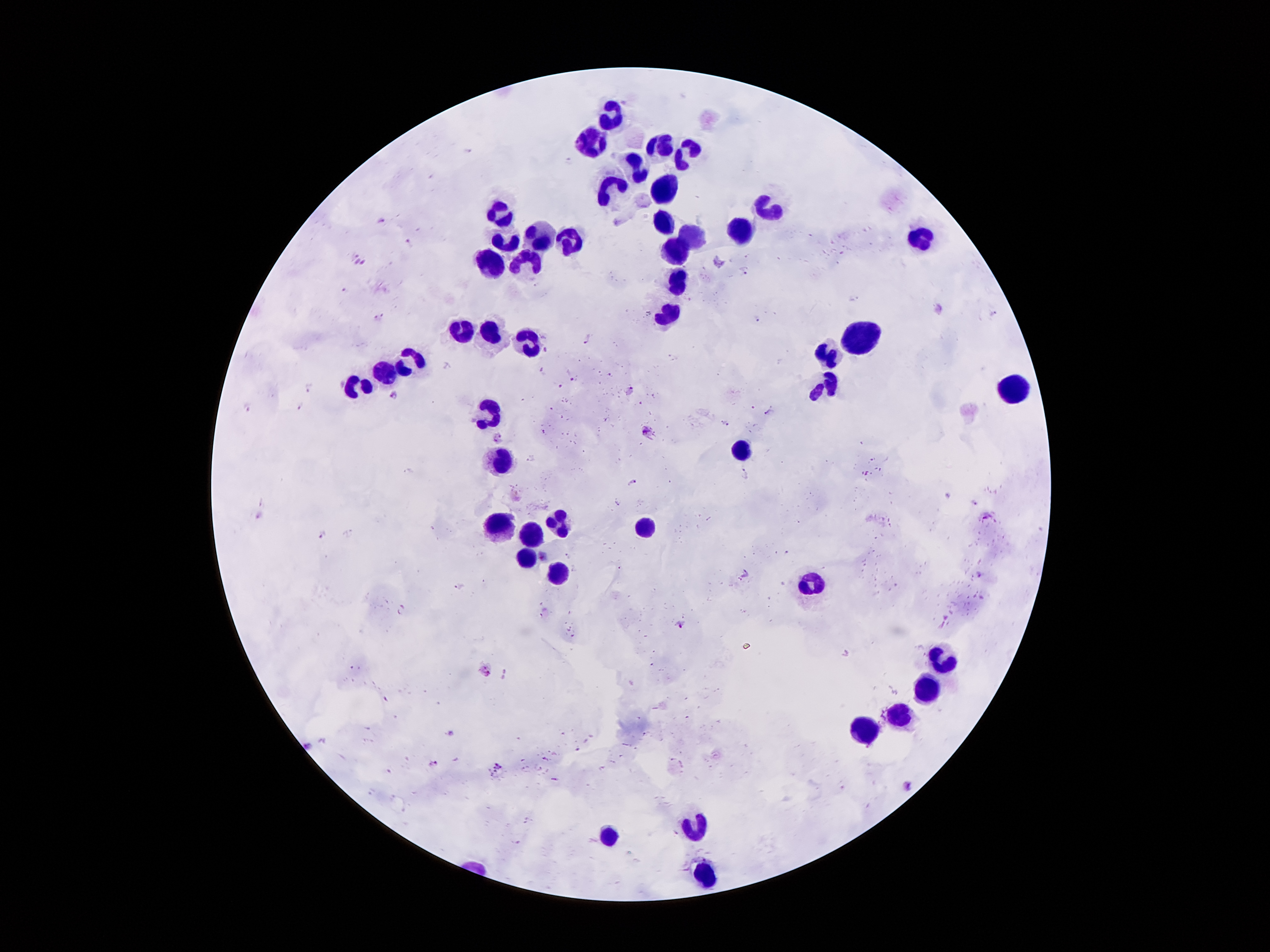

Approximate centers as {x, y} in pixels. Malaria parasite locations: {381, 221}, {408, 242}, {745, 270}, {380, 316}, {587, 338}, {572, 379}, {311, 385}, {560, 387}, {630, 389}, {393, 394}, {248, 408}, {302, 409}, {769, 413}, {727, 424}, {543, 431}, {646, 431}, {498, 437}, {632, 482}, {617, 503}, {259, 514}, {321, 535}, {543, 558}, {681, 624}, {487, 670}, {308, 746}, {435, 764}, {498, 766}, {908, 785}. Leukocyte locations: {616, 115}, {662, 142}, {589, 143}, {697, 151}, {638, 167}, {610, 184}, {674, 190}, {500, 206}, {769, 210}, {667, 223}, {541, 231}, {739, 231}, {695, 233}, {925, 239}, {506, 242}, {571, 242}, {674, 251}, {529, 260}, {493, 266}, {682, 284}, {667, 318}, {470, 328}, {496, 338}, {857, 340}, {527, 341}, {833, 348}, {409, 364}, {388, 374}, {356, 384}, {824, 386}, {1013, 393}, {494, 410}, {742, 447}, {502, 458}, {565, 523}, {502, 527}, {643, 527}, {530, 532}, {526, 558}, {557, 579}, {815, 585}, {944, 661}, {926, 687}, {902, 713}, {863, 731}, {701, 827}, {613, 838}, {706, 872}. Patient malaria status: positive for Plasmodium falciparum. 100x magnification. One field from this slide. Giemsa-stained preparation. Image is 1270×952 pixels. Thick blood smear. Photographed through the microscope eyepiece with a smartphone camera.